State which cell type is depicted.
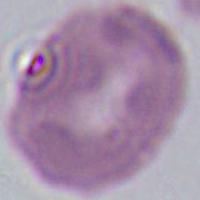

This is an erythrocyte.

Summary:
  - Magnification: 1000x
  - Modality: micrograph